Describe the morphology of the red blood cells.
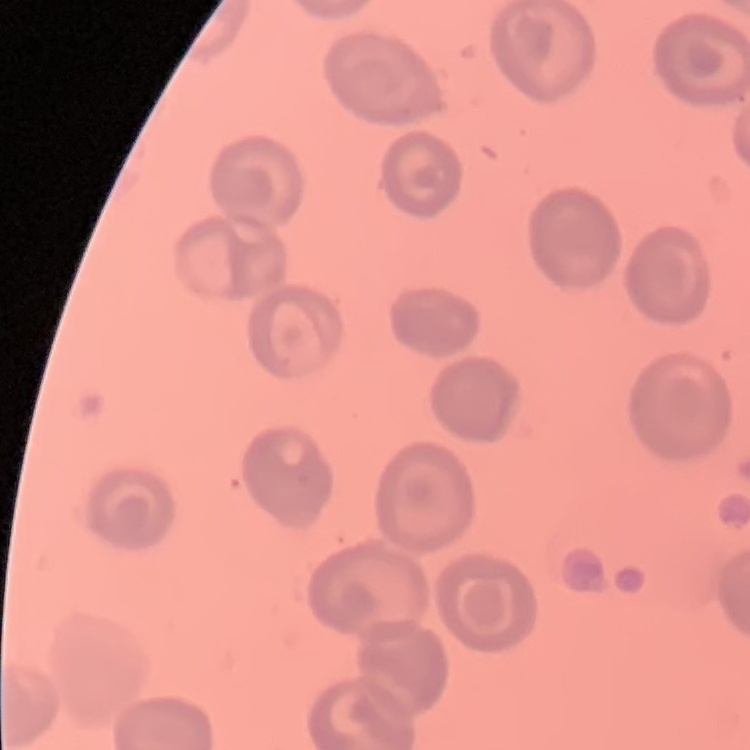

They show no rouleaux formation.

Summary:
  - Image type: square crop of a larger photomicrograph
  - Preparation: thin blood film
  - Stain: Field's or Giemsa